Outline each blood parasite and name the species.
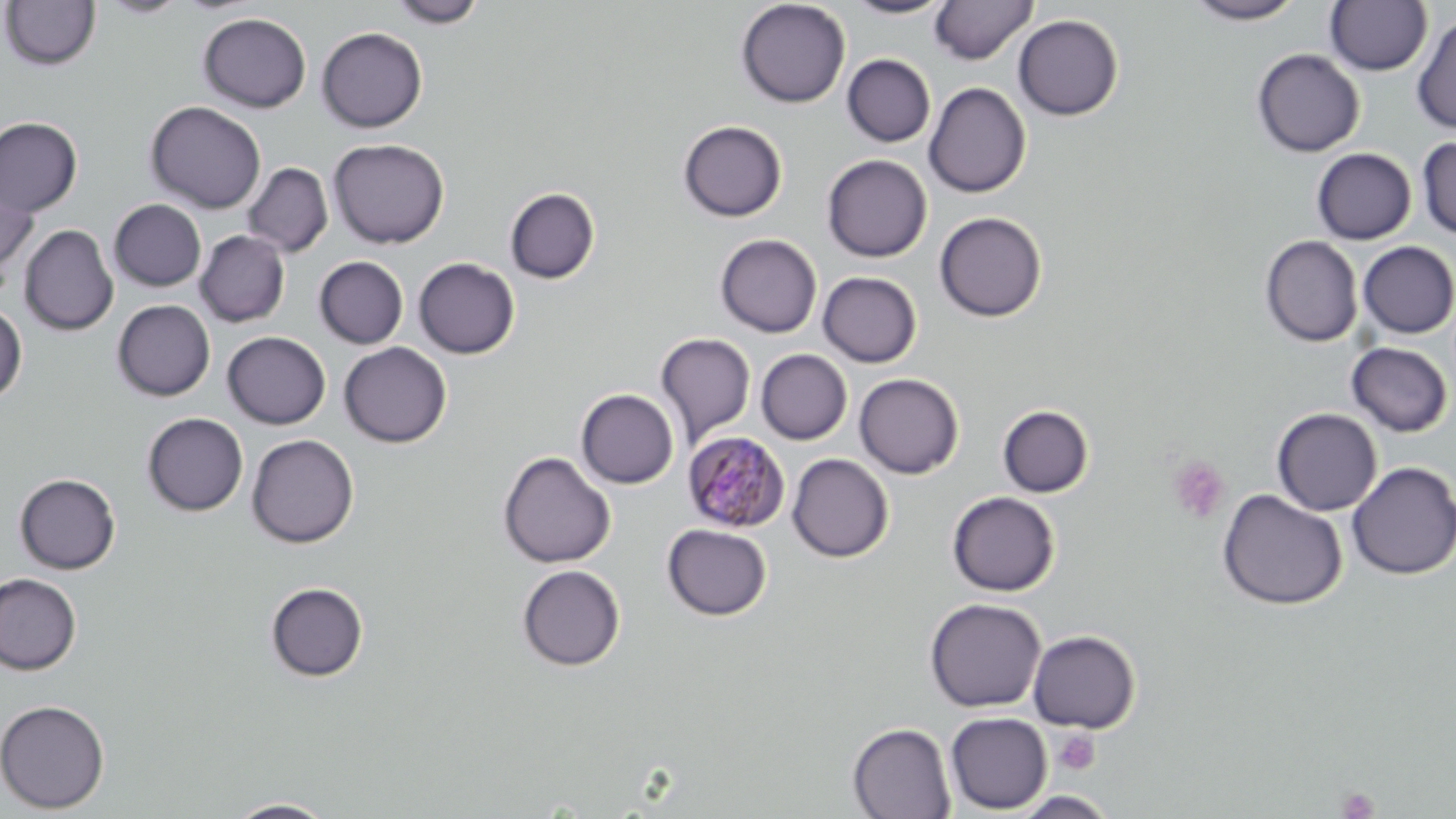
Approximate bounding boxes as (x1, y1, x2, y2) in pixels.
Plasmodium malariae-infected red blood cells: (684, 432, 791, 533).
No Plasmodium falciparum, Plasmodium ovale, Plasmodium vivax, Babesia divergens, or Trypanosoma brucei observed.

Uninfected red blood cell locations: (98, 0, 189, 18), (389, 0, 487, 28), (736, 0, 851, 108), (844, 0, 954, 19), (929, 0, 1038, 65), (1185, 0, 1304, 24), (1, 1, 100, 72), (1325, 1, 1433, 76), (198, 12, 312, 112), (1412, 12, 1456, 134), (1012, 14, 1124, 121), (316, 27, 427, 132), (1251, 49, 1365, 157), (842, 54, 936, 147), (923, 82, 1032, 198), (145, 101, 266, 214), (0, 116, 83, 217), (678, 120, 787, 222), (1416, 136, 1456, 239), (328, 138, 450, 248), (1312, 148, 1416, 244), (822, 154, 932, 262), (243, 162, 333, 257), (1, 167, 39, 284), (505, 187, 600, 284), (109, 199, 207, 292), (934, 211, 1047, 322), (19, 224, 119, 336), (195, 230, 290, 327), (715, 234, 822, 338), (1260, 235, 1362, 347), (1357, 241, 1456, 338), (314, 256, 409, 349), (413, 257, 520, 359), (817, 271, 922, 367), (112, 300, 215, 401), (0, 303, 27, 405), (222, 331, 330, 429), (655, 333, 756, 446), (1346, 341, 1453, 437), (338, 342, 452, 448), (756, 349, 853, 445), (854, 373, 964, 478), (576, 389, 679, 489), (997, 404, 1094, 498), (1272, 407, 1382, 515), (142, 413, 249, 516), (246, 434, 359, 548), (498, 451, 615, 568), (787, 453, 894, 562), (1346, 461, 1456, 580), (14, 473, 121, 574), (1217, 489, 1347, 610), (946, 491, 1060, 596), (662, 523, 772, 621), (516, 564, 626, 671), (0, 573, 82, 675), (265, 581, 369, 682), (924, 597, 1047, 713), (1028, 629, 1141, 733), (0, 699, 111, 814), (945, 712, 1052, 814), (847, 722, 956, 819), (225, 798, 337, 818). Platelet locations: (1167, 455, 1231, 524), (1053, 729, 1100, 775), (1336, 786, 1379, 819). Slide-level diagnosis: Plasmodium malariae. Thin blood smear. Image is 1456×819 pixels. Optical microscopy. Captured at 1000x magnification. One field of a larger specimen. May-Grünwald-Giemsa-stained preparation.